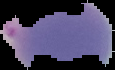

preparation = thin blood film
result = no Plasmodium parasites seen
image type = segmented cell region with the area outside set to black
image size = 115×70 pixels